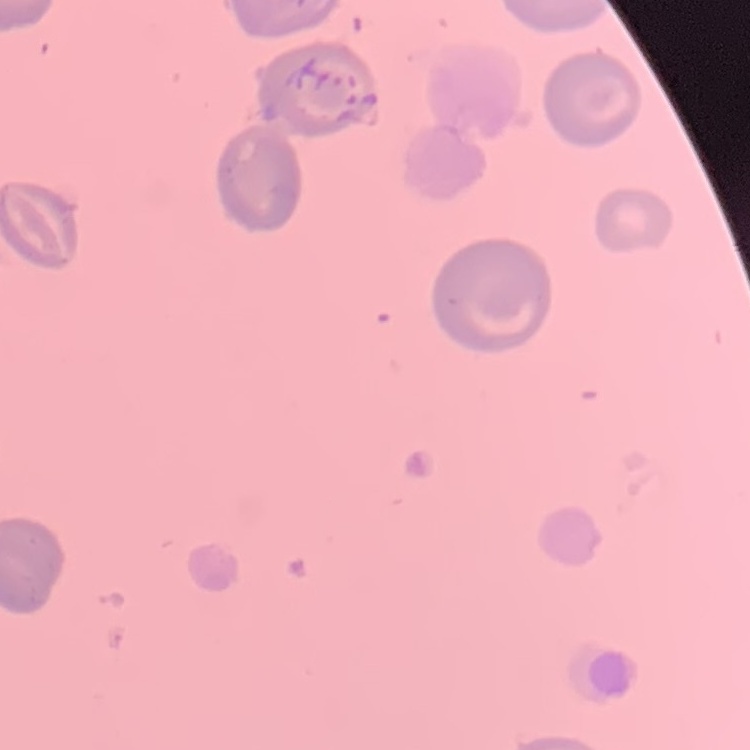

The erythrocytes show no rouleaux formation. Thin peripheral smear. Stained with either Field's or Giemsa. Square crop of a larger photomicrograph.